Assess this cell for malaria.
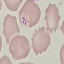

Uninfected.

Summary:
  - Preparation: thin blood smear
  - Capture: smartphone through the microscope eyepiece
  - Image type: automatically extracted cell patch, resized to 64 × 64 pixels
  - Stain: Giemsa